Assess this cell for malaria.
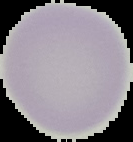

Uninfected.

image type = segmented cell region with the area outside set to black
image size = 133×142 pixels
preparation = thin blood film